Outline every leukocyte.
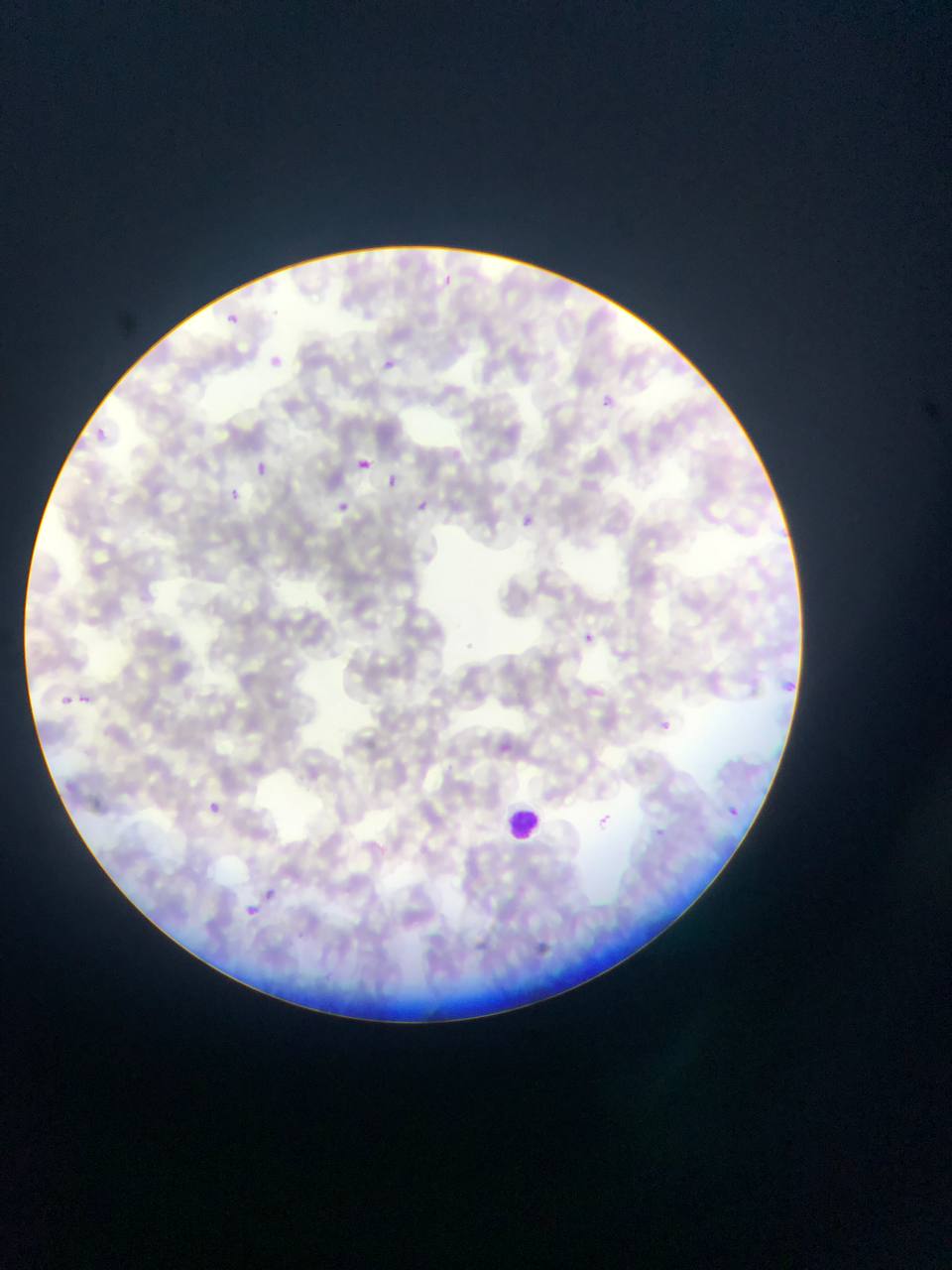

Approximate bounding boxes as [left, top, right, bottom] in pixels.
Leukocytes: [504, 804, 547, 844].

Summary:
  - Malaria parasite locations (subset; some below the resolvable size): [445, 272, 462, 289], [226, 312, 244, 331], [268, 350, 288, 366], [383, 358, 408, 376], [599, 393, 612, 417], [92, 426, 110, 441], [359, 455, 381, 477], [255, 460, 269, 475], [390, 466, 404, 486], [229, 489, 239, 500], [416, 495, 438, 516], [334, 498, 356, 516], [521, 510, 537, 523], [580, 626, 596, 645], [783, 677, 796, 692], [55, 691, 76, 709], [78, 693, 92, 704], [656, 711, 671, 733], [500, 737, 525, 760], [209, 802, 221, 815], [731, 803, 744, 819], [598, 809, 618, 831], [265, 880, 287, 910], [237, 899, 262, 917]
  - Image size: 952×1270 pixels
  - Field of view: single
  - Preparation: thin blood smear
  - Capture: mobile-phone photograph through a microscope
  - Country: Ghana